Report the malaria status of this cell.
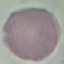

It is uninfected.

Giemsa-stained preparation. Automatically extracted cell patch, resized to 64 × 64 pixels. Thin blood film. Photographed with a smartphone camera at the microscope eyepiece.